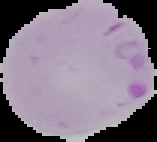
Malaria status: parasitized. Cell region segmented out of the field of view; the surrounding area is masked to black. Image is 157×142 pixels. From a thin blood smear.